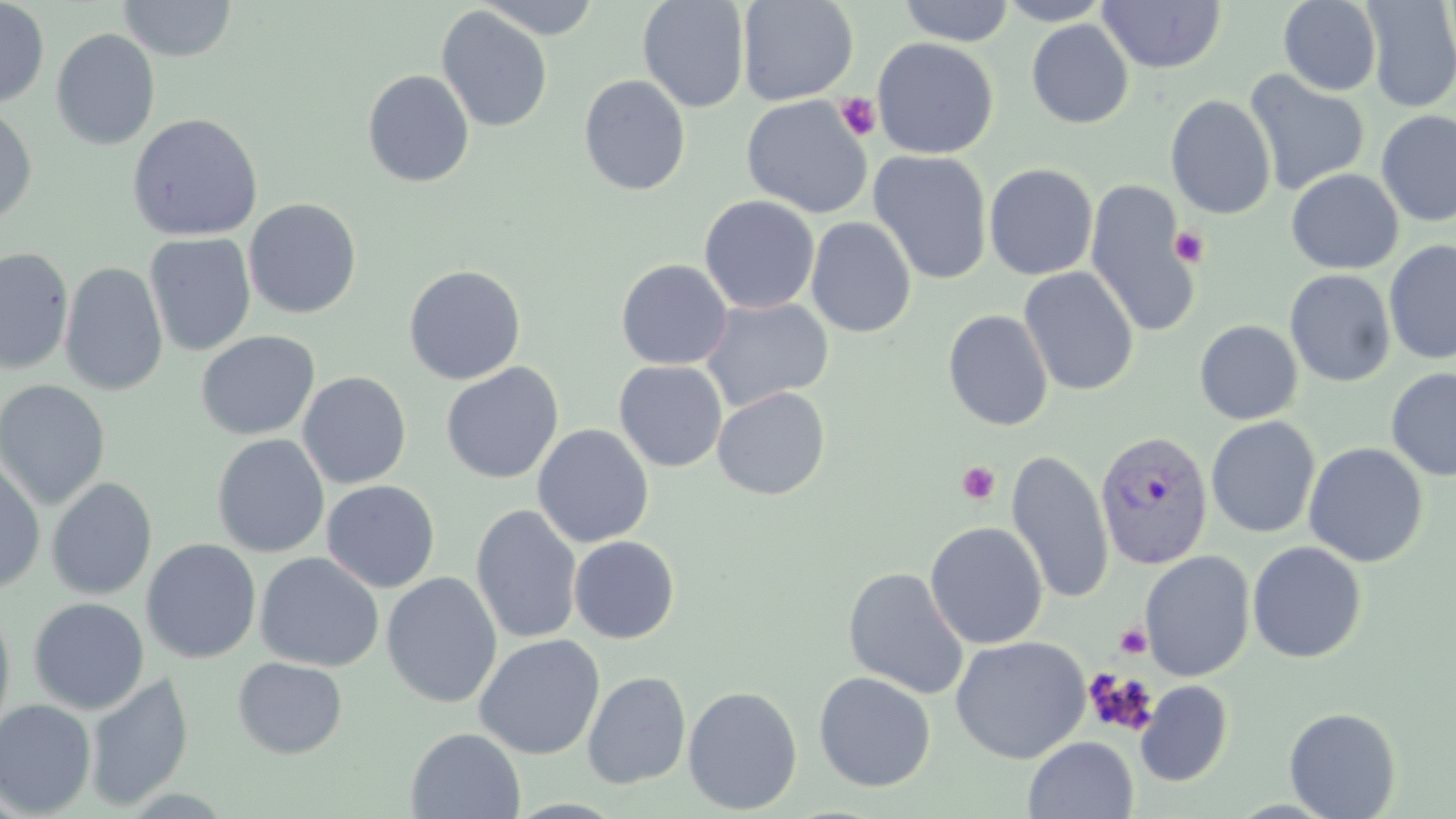
Summary:
  - Coordinate format: approximate bounding boxes as named x1/y1/x2/y2 corners in pixels
  - Plasmodium vivax-infected red blood cell locations: (x1=1093, y1=431, x2=1214, y2=570)
  - Uninfected red blood cell locations: (x1=118, y1=0, x2=237, y2=61), (x1=476, y1=0, x2=603, y2=40), (x1=637, y1=0, x2=751, y2=113), (x1=737, y1=0, x2=859, y2=106), (x1=995, y1=0, x2=1114, y2=25), (x1=1278, y1=0, x2=1382, y2=96), (x1=0, y1=1, x2=50, y2=108), (x1=898, y1=1, x2=1016, y2=46), (x1=1097, y1=1, x2=1227, y2=73), (x1=1361, y1=1, x2=1456, y2=112), (x1=436, y1=6, x2=553, y2=133), (x1=1026, y1=19, x2=1134, y2=129), (x1=50, y1=28, x2=160, y2=151), (x1=872, y1=37, x2=999, y2=159), (x1=362, y1=69, x2=475, y2=187), (x1=1243, y1=71, x2=1369, y2=196), (x1=579, y1=74, x2=691, y2=195), (x1=740, y1=95, x2=873, y2=218), (x1=1165, y1=95, x2=1276, y2=219), (x1=0, y1=105, x2=38, y2=225), (x1=1376, y1=110, x2=1456, y2=227), (x1=127, y1=112, x2=264, y2=242), (x1=868, y1=149, x2=993, y2=285), (x1=984, y1=163, x2=1098, y2=280), (x1=1286, y1=168, x2=1403, y2=274), (x1=1085, y1=179, x2=1200, y2=339), (x1=699, y1=195, x2=820, y2=314), (x1=244, y1=198, x2=362, y2=318), (x1=805, y1=216, x2=917, y2=338), (x1=144, y1=233, x2=256, y2=356), (x1=1384, y1=240, x2=1456, y2=364), (x1=0, y1=247, x2=75, y2=375), (x1=615, y1=258, x2=733, y2=370), (x1=60, y1=262, x2=168, y2=397), (x1=403, y1=264, x2=527, y2=385), (x1=1019, y1=267, x2=1139, y2=396), (x1=1284, y1=269, x2=1396, y2=387), (x1=700, y1=297, x2=834, y2=412), (x1=942, y1=309, x2=1054, y2=431), (x1=1194, y1=320, x2=1303, y2=425), (x1=195, y1=330, x2=320, y2=441), (x1=614, y1=361, x2=728, y2=471), (x1=441, y1=362, x2=563, y2=484), (x1=1386, y1=368, x2=1456, y2=481), (x1=297, y1=371, x2=411, y2=489), (x1=0, y1=380, x2=111, y2=510), (x1=712, y1=386, x2=831, y2=500), (x1=1206, y1=416, x2=1321, y2=538), (x1=533, y1=424, x2=654, y2=548), (x1=211, y1=433, x2=330, y2=557), (x1=1303, y1=442, x2=1428, y2=567), (x1=1006, y1=448, x2=1114, y2=605), (x1=0, y1=456, x2=45, y2=594), (x1=46, y1=477, x2=158, y2=600), (x1=321, y1=479, x2=441, y2=593), (x1=471, y1=504, x2=583, y2=644), (x1=925, y1=521, x2=1048, y2=650), (x1=568, y1=535, x2=680, y2=644), (x1=141, y1=538, x2=262, y2=664), (x1=1247, y1=541, x2=1367, y2=663), (x1=254, y1=551, x2=384, y2=671), (x1=1139, y1=551, x2=1256, y2=681), (x1=843, y1=567, x2=970, y2=700), (x1=381, y1=572, x2=503, y2=708), (x1=28, y1=597, x2=149, y2=714), (x1=0, y1=601, x2=16, y2=743), (x1=474, y1=634, x2=606, y2=760), (x1=949, y1=635, x2=1091, y2=763), (x1=232, y1=656, x2=348, y2=759), (x1=582, y1=671, x2=691, y2=789), (x1=813, y1=671, x2=936, y2=792), (x1=85, y1=672, x2=194, y2=812), (x1=1135, y1=680, x2=1233, y2=787), (x1=682, y1=685, x2=803, y2=815), (x1=0, y1=698, x2=97, y2=817), (x1=1284, y1=707, x2=1402, y2=819), (x1=406, y1=728, x2=526, y2=818), (x1=1022, y1=735, x2=1138, y2=818)
  - Platelet locations: (x1=835, y1=92, x2=881, y2=141), (x1=1169, y1=227, x2=1209, y2=268), (x1=957, y1=461, x2=1001, y2=505), (x1=1114, y1=623, x2=1152, y2=659), (x1=1083, y1=668, x2=1158, y2=736)
  - Slide-level diagnosis: Plasmodium vivax
  - Stain: May-Grünwald-Giemsa
  - Preparation: thin blood smear
  - Modality: optical microscopy
  - Field of view: single
  - Magnification: 1000x
  - Image size: 1456×819 pixels